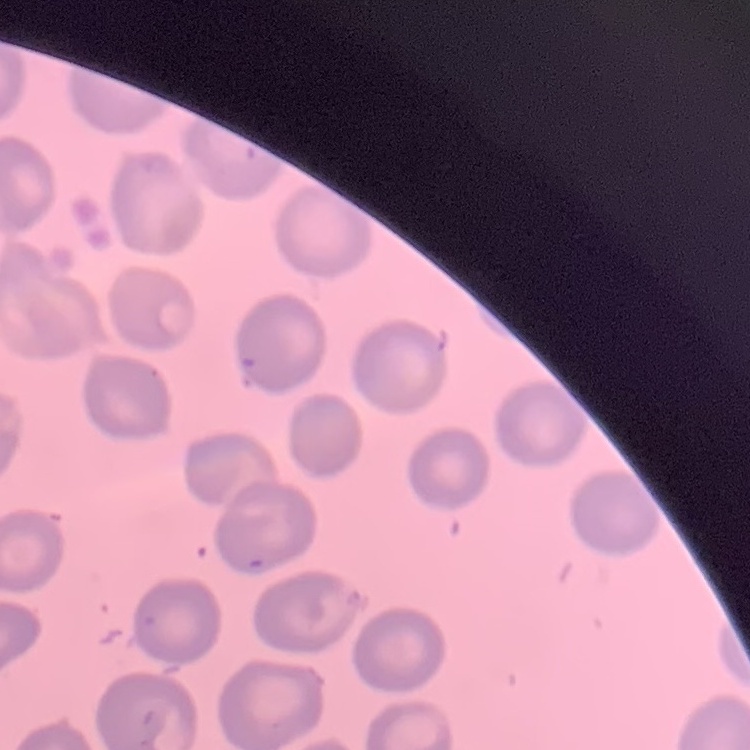
The red blood cells show no rouleaux formation. Thin blood smear. Square crop of a larger photomicrograph. Stained with either Field's or Giemsa.